Assess this cell for malaria.
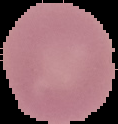

Uninfected.

{
  "preparation": "thin blood smear",
  "image_size": "118×124 pixels",
  "image_type": "segmented cell region on a black background"
}